Describe the morphology of the red blood cells.
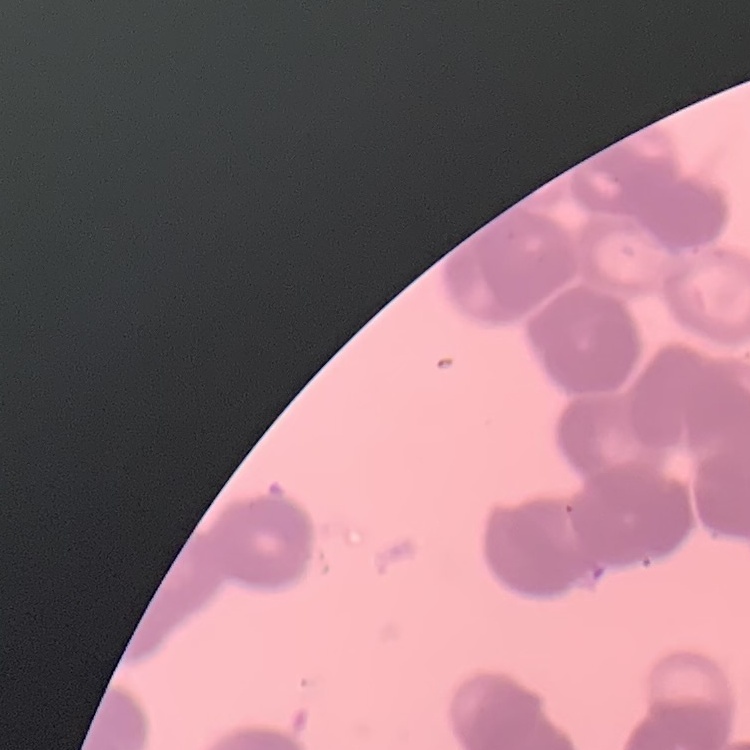

They show rouleaux formation.

Summary:
  - Stain: Field's or Giemsa
  - Image type: one tile cut from a larger photomicrograph
  - Preparation: thin blood film